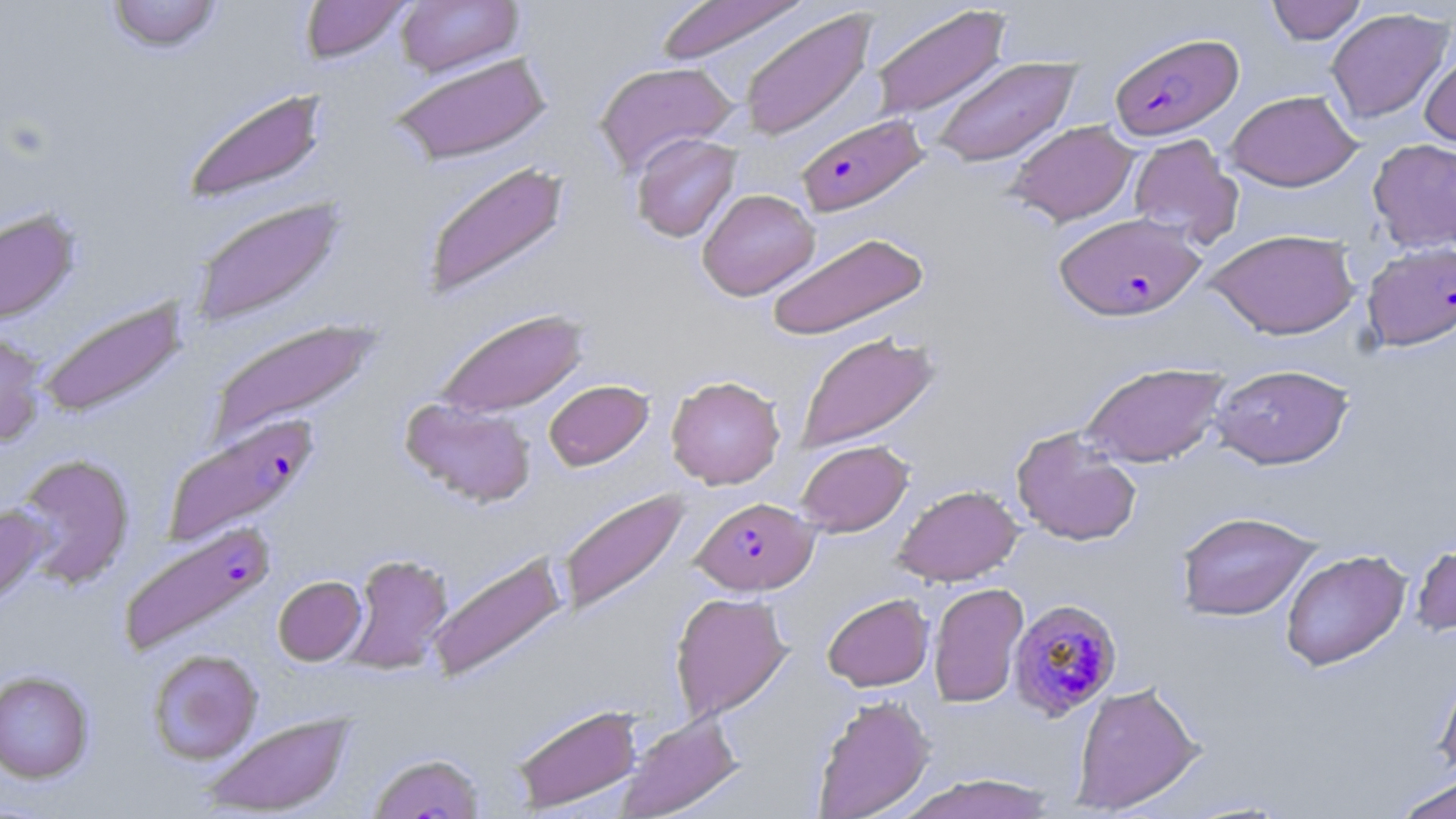

Approximate bounding boxes as named x1/y1/x2/y2 corners in pixels. Plasmodium falciparum-infected red blood cell locations: (x1=1109, y1=31, x2=1243, y2=140), (x1=796, y1=113, x2=930, y2=217), (x1=1054, y1=212, x2=1206, y2=322), (x1=1361, y1=241, x2=1456, y2=351), (x1=162, y1=415, x2=320, y2=545), (x1=692, y1=497, x2=818, y2=595), (x1=119, y1=520, x2=276, y2=655), (x1=1010, y1=598, x2=1124, y2=719). Uninfected red blood cell locations: (x1=106, y1=0, x2=223, y2=53), (x1=299, y1=0, x2=411, y2=62), (x1=395, y1=0, x2=523, y2=77), (x1=655, y1=0, x2=810, y2=67), (x1=1266, y1=0, x2=1366, y2=45), (x1=869, y1=4, x2=1012, y2=121), (x1=738, y1=7, x2=877, y2=142), (x1=1325, y1=8, x2=1453, y2=124), (x1=1420, y1=48, x2=1456, y2=152), (x1=389, y1=52, x2=554, y2=166), (x1=930, y1=56, x2=1081, y2=168), (x1=594, y1=61, x2=739, y2=175), (x1=182, y1=87, x2=329, y2=205), (x1=1225, y1=90, x2=1361, y2=191), (x1=1006, y1=120, x2=1138, y2=225), (x1=631, y1=132, x2=742, y2=243), (x1=1128, y1=134, x2=1242, y2=248), (x1=1368, y1=138, x2=1456, y2=252), (x1=421, y1=160, x2=572, y2=301), (x1=697, y1=188, x2=820, y2=300), (x1=190, y1=196, x2=347, y2=329), (x1=0, y1=209, x2=80, y2=326), (x1=1206, y1=228, x2=1360, y2=339), (x1=766, y1=231, x2=930, y2=342), (x1=37, y1=295, x2=188, y2=419), (x1=433, y1=308, x2=590, y2=419), (x1=207, y1=317, x2=382, y2=442), (x1=0, y1=329, x2=48, y2=447), (x1=794, y1=332, x2=941, y2=454), (x1=1080, y1=362, x2=1229, y2=467), (x1=1210, y1=363, x2=1354, y2=469), (x1=666, y1=375, x2=785, y2=489), (x1=543, y1=379, x2=653, y2=470), (x1=399, y1=397, x2=537, y2=508), (x1=1011, y1=427, x2=1142, y2=546), (x1=795, y1=440, x2=913, y2=536), (x1=14, y1=453, x2=136, y2=589), (x1=893, y1=484, x2=1023, y2=586), (x1=558, y1=489, x2=690, y2=616), (x1=0, y1=503, x2=51, y2=609), (x1=1176, y1=511, x2=1321, y2=621), (x1=1410, y1=537, x2=1456, y2=637), (x1=1280, y1=549, x2=1410, y2=671), (x1=426, y1=551, x2=568, y2=684), (x1=343, y1=553, x2=454, y2=674), (x1=273, y1=575, x2=366, y2=665), (x1=928, y1=582, x2=1029, y2=708), (x1=669, y1=591, x2=793, y2=722), (x1=822, y1=593, x2=934, y2=691), (x1=147, y1=648, x2=263, y2=764), (x1=1434, y1=663, x2=1456, y2=783), (x1=0, y1=670, x2=95, y2=783), (x1=1071, y1=681, x2=1204, y2=815), (x1=812, y1=694, x2=935, y2=819), (x1=510, y1=704, x2=643, y2=812), (x1=201, y1=712, x2=356, y2=816), (x1=615, y1=712, x2=744, y2=819), (x1=367, y1=751, x2=486, y2=819), (x1=897, y1=773, x2=1059, y2=818), (x1=1391, y1=773, x2=1456, y2=819). Slide-level diagnosis: Plasmodium falciparum. Thin blood film. 1000x magnification. Image is 1456×819 pixels. May-Grünwald-Giemsa-stained preparation. Single field of view. Light microscopy.